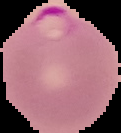

malaria status = parasitized
image type = segmented cell region with the area outside set to black
preparation = thin blood smear
image size = 121×133 pixels